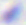 400x magnification. Micrograph. Toxoplasma gondii is seen.